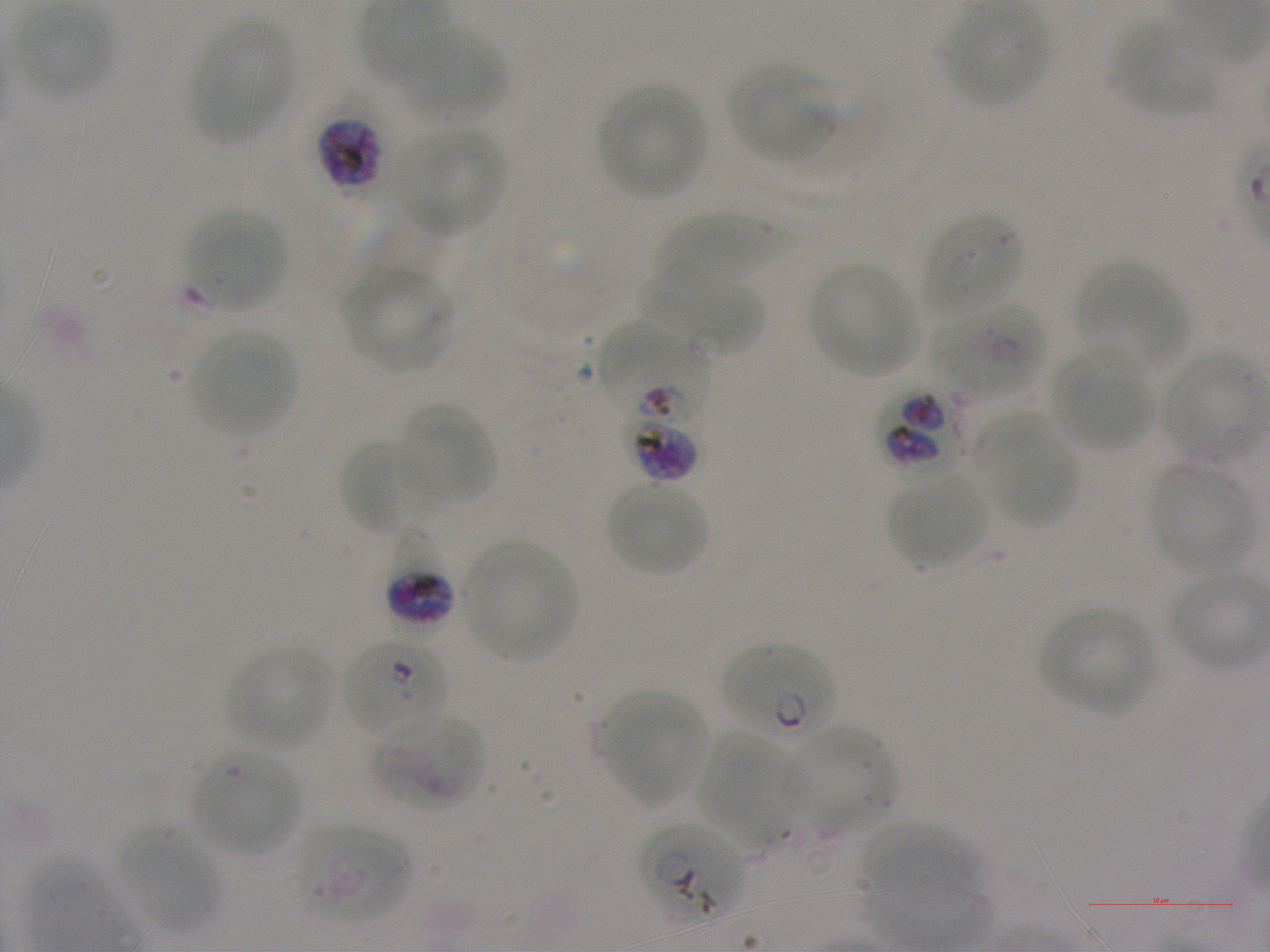
Approximate bounding boxes as [x1, y1, x2, y2] in pixels. Not every red blood cell is marked. A life-cycle stage — or a range of stages, where the recorded stages span more than one — follows each staged infected red blood cell. Locations of red blood cells of indeterminate infection status: [924, 214, 1021, 317], [645, 276, 763, 357], [929, 300, 1045, 400], [600, 319, 711, 416], [621, 386, 703, 483], [373, 714, 485, 810], [295, 825, 408, 921]. Locations of infected red blood cells: [318, 118, 384, 192] schizont; [880, 385, 969, 478]; [385, 527, 455, 623]; [343, 640, 449, 742] ring; [720, 643, 837, 744] ring; [641, 821, 747, 921]. Locations of uninfected red blood cells: [947, 5, 1051, 106], [19, 7, 114, 98], [189, 20, 293, 140], [1116, 21, 1220, 115], [403, 28, 507, 120], [731, 65, 836, 163], [597, 86, 707, 197], [401, 128, 505, 235], [187, 210, 288, 310], [658, 213, 780, 285], [810, 263, 919, 376], [1079, 264, 1188, 373], [343, 265, 456, 372], [188, 329, 298, 435], [1052, 350, 1153, 452], [1159, 351, 1265, 459], [397, 403, 497, 507], [991, 433, 1080, 529], [340, 439, 422, 535], [1149, 462, 1253, 574], [889, 471, 988, 568], [608, 482, 709, 577], [463, 540, 576, 658], [1039, 606, 1156, 712], [230, 647, 332, 749], [603, 691, 707, 803], [784, 726, 899, 834], [698, 729, 799, 850], [192, 750, 301, 854], [862, 823, 978, 916], [120, 827, 219, 931]. Life-cycle stages observed: ring, schizont. Image is 1270×952 pixels. Thin blood smear. Plasmodium falciparum strain NF54 maintained in static in-vitro culture. One field from this slide. 100x objective under oil immersion, numerical aperture 1.25. Giemsa-stained preparation. Blood group of the donor: A+.